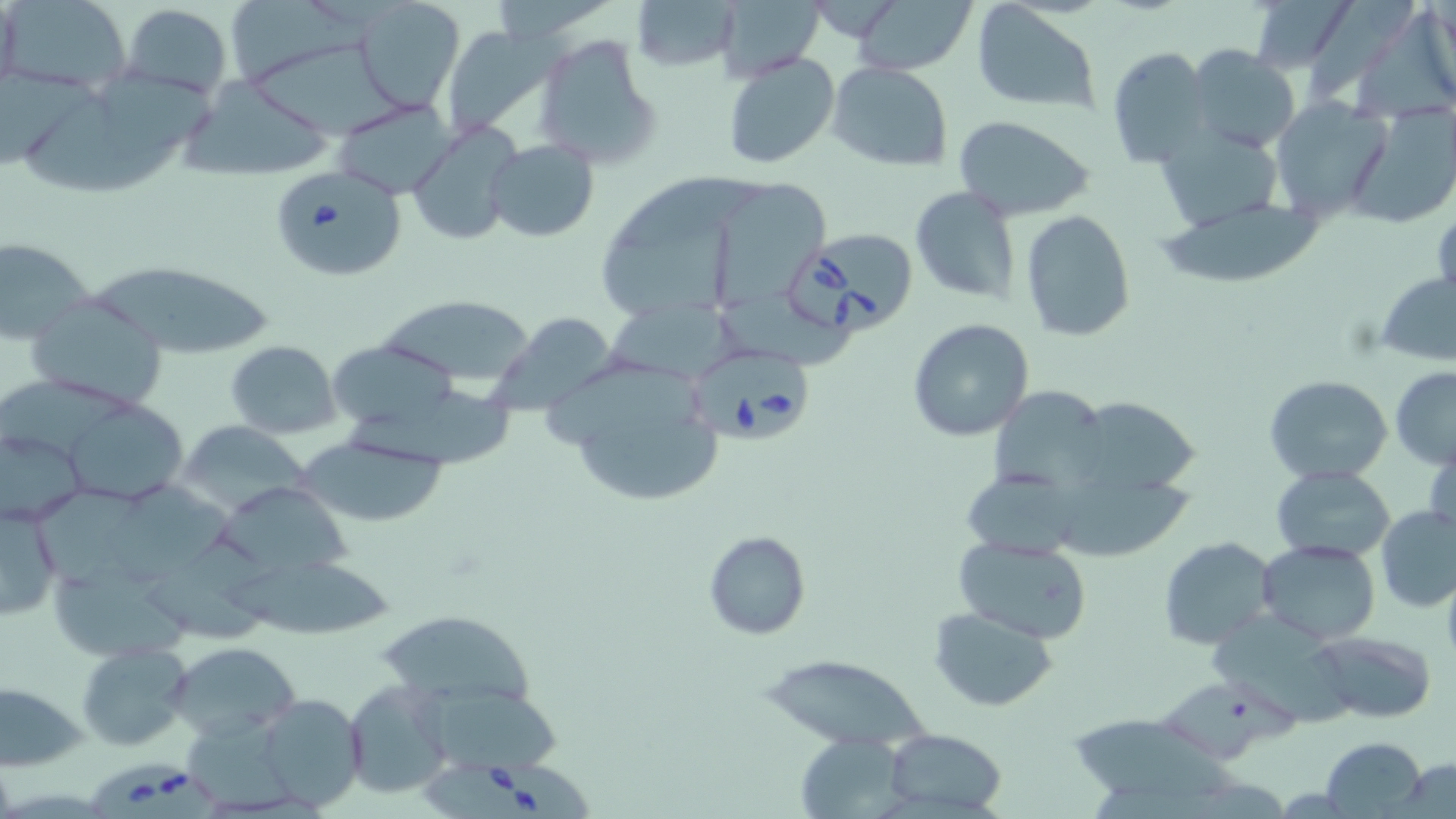

slide_level_diagnosis: Babesia divergens
modality: light microscopy
stain: May-Grünwald-Giemsa
babesia_divergens_infected_red_blood_cell_locations: 'approximate bounding boxes as (x1, y1, x2, y2) in pixels: (267, 164, 406, 283), (786, 224, 914, 335), (692, 341, 816, 445), (421, 755, 597, 819), (89, 760, 219, 819)'
magnification: 1000x
image_size: 1456×819 pixels
preparation: thin blood film
field_of_view: one of a larger specimen
uninfected_red_blood_cell_locations: 'approximate bounding boxes as (x1, y1, x2, y2) in pixels: (0, 0, 133, 93), (355, 0, 465, 111), (627, 0, 740, 73), (844, 0, 980, 74), (1250, 0, 1356, 75), (1305, 0, 1416, 99), (235, 1, 375, 85), (120, 2, 234, 99), (716, 2, 825, 78), (972, 4, 1098, 115), (1357, 13, 1456, 115), (439, 25, 556, 138), (534, 34, 662, 169), (252, 43, 407, 141), (1106, 46, 1212, 168), (1188, 46, 1300, 155), (720, 51, 840, 170), (825, 62, 953, 170), (0, 67, 101, 169), (98, 67, 227, 152), (184, 79, 337, 183), (30, 95, 180, 190), (1270, 97, 1394, 223), (332, 99, 455, 198), (1354, 103, 1456, 223), (951, 114, 1099, 222), (407, 121, 519, 245), (1154, 124, 1284, 230), (484, 139, 599, 241), (715, 178, 825, 306), (909, 185, 1023, 305), (1161, 197, 1327, 288), (603, 205, 735, 319), (1020, 209, 1137, 343), (0, 236, 96, 343), (85, 255, 276, 357), (1374, 268, 1456, 369), (378, 295, 538, 389), (724, 296, 863, 371), (27, 297, 167, 412), (489, 303, 627, 414), (602, 304, 741, 382), (907, 318, 1034, 441), (323, 338, 459, 437), (226, 340, 341, 439), (549, 361, 729, 508), (1391, 365, 1456, 469), (0, 374, 132, 460), (1264, 374, 1392, 485), (988, 383, 1111, 497), (346, 386, 514, 469), (1068, 396, 1204, 503), (67, 399, 186, 503), (174, 420, 310, 515), (0, 429, 88, 525), (1426, 430, 1456, 546), (301, 437, 449, 526), (1269, 464, 1397, 563), (962, 468, 1085, 559), (108, 473, 238, 581), (215, 478, 366, 577), (1061, 478, 1198, 561), (36, 483, 161, 590), (1, 503, 62, 622), (1376, 505, 1456, 613), (703, 531, 810, 639), (153, 532, 280, 643), (953, 536, 1095, 644), (1157, 536, 1278, 649), (1256, 539, 1382, 642), (223, 562, 398, 639), (54, 567, 197, 662), (928, 606, 1061, 711), (376, 610, 543, 708), (1209, 614, 1361, 728), (1309, 630, 1435, 723), (167, 641, 301, 739), (79, 643, 193, 750), (761, 652, 931, 752), (1164, 674, 1296, 767), (409, 675, 564, 779), (342, 677, 455, 801), (0, 683, 87, 771), (258, 692, 365, 812), (184, 707, 300, 811), (1071, 709, 1241, 797), (882, 727, 1007, 816), (796, 732, 909, 816), (1321, 736, 1428, 816), (1393, 759, 1456, 816)'